Classify this cell by malaria status.
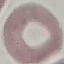
Uninfected.

Automatically extracted cell patch, resized to 64 × 64 pixels. Acquired by smartphone through the microscope eyepiece. Thin blood smear. Giemsa stain.